Locate every Plasmodium parasite.
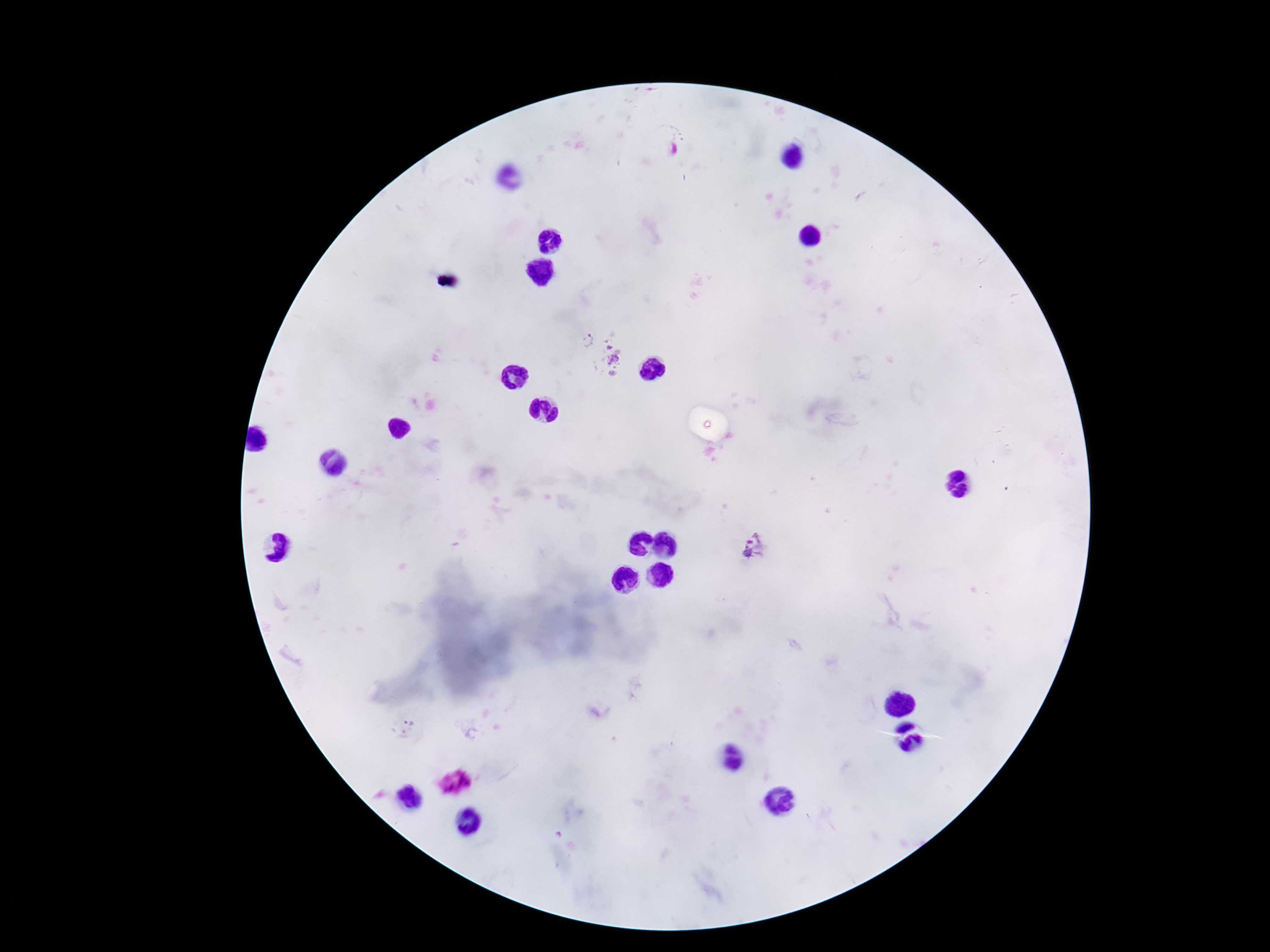
Approximate centers as [x, y] in pixels.
Plasmodium parasites: [586, 338], [612, 359], [755, 547], [405, 728].

Summary:
  - Capture: smartphone camera through the microscope eyepiece
  - Patient malaria status: positive
  - Image size: 1270×952 pixels
  - Magnification: 100x
  - Field of view: single
  - Preparation: thick peripheral-blood smear
  - Stain: Giemsa